Assess the morphology of the erythrocytes.
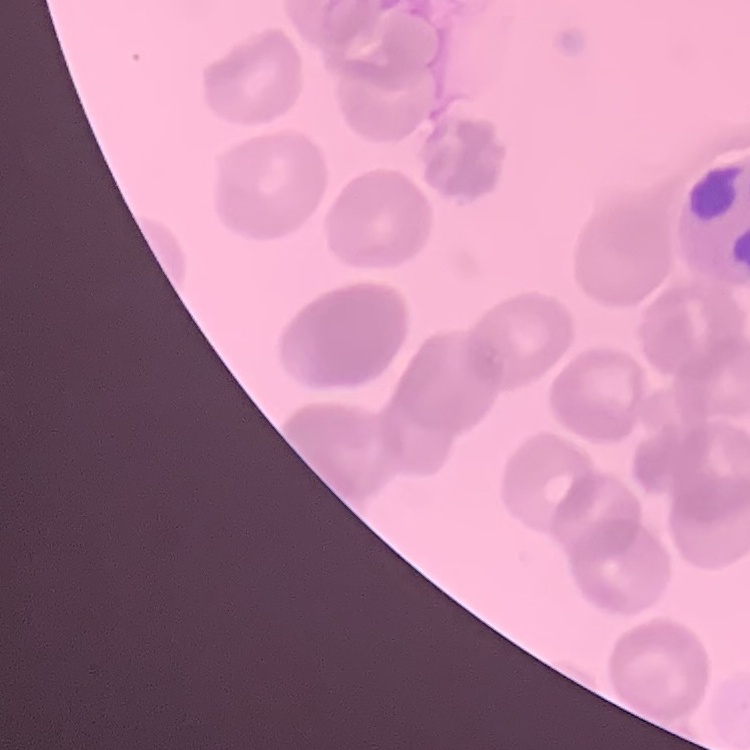

They show rouleaux formation.

Square crop of a larger photomicrograph. Thin blood film. Stained with either Field's or Giemsa.